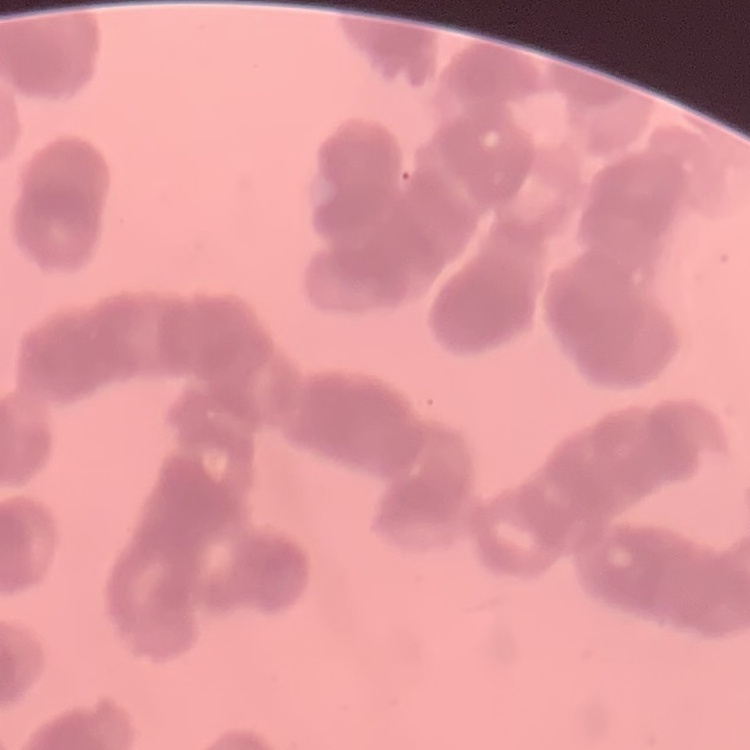

Summary:
  - Erythrocyte morphology: rouleaux formation
  - Preparation: thin peripheral smear
  - Image type: one tile cut from a larger photomicrograph
  - Stain: Field's or Giemsa